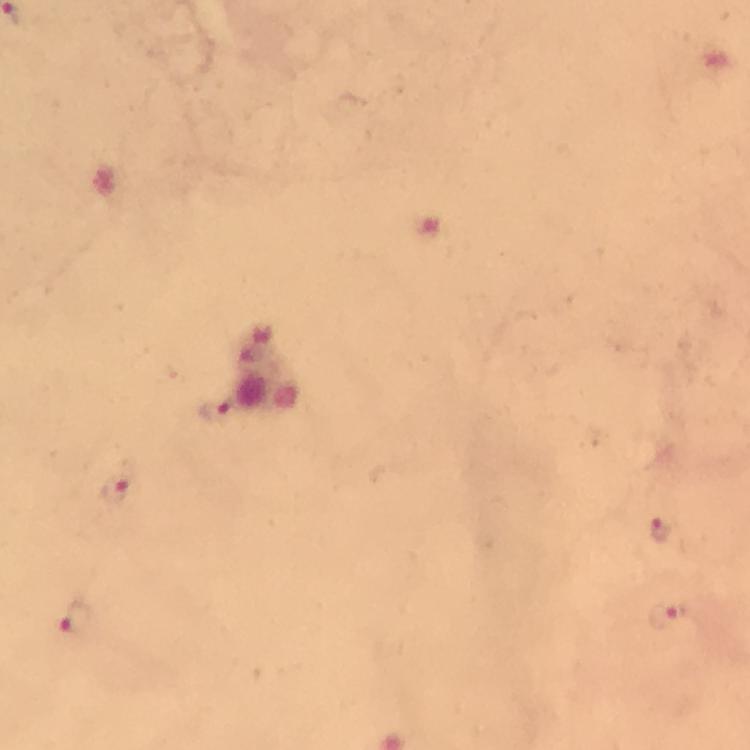
image_size: 750×750 pixels
magnification: 100x
immersion_oil: applied
context: from a malaria diagnostic workup
preparation: thick smear
capture: smartphone photograph through a microscope
stain: Giemsa
plasmodium_parasite_locations: 'approximate centers as {x, y} in pixels: {118, 488}, {662, 530}, {664, 614}, {79, 618}'
cropped_from: a single field of view